Give the position of every Plasmodium parasite.
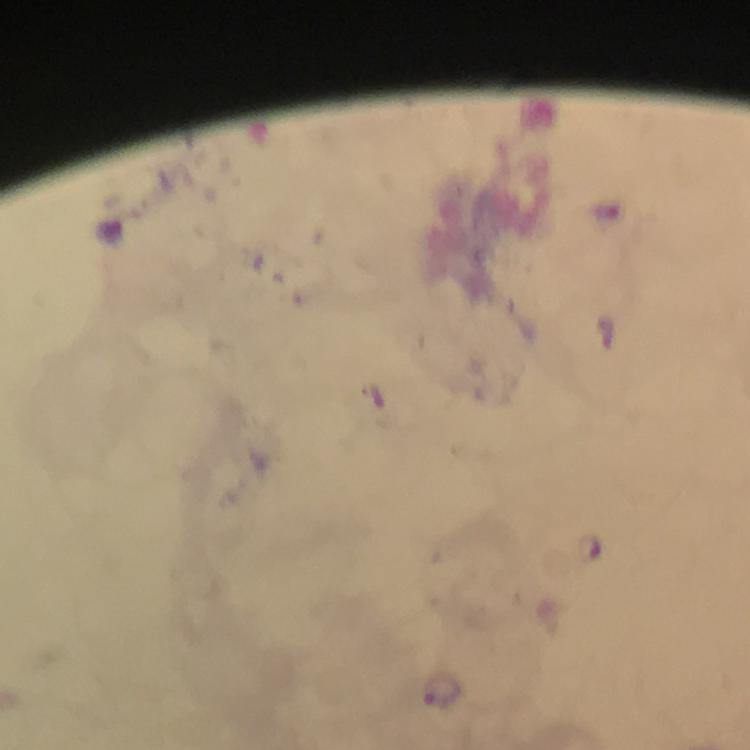

Approximate centers as [x, y] in pixels.
Plasmodium parasites: [441, 691].

cropped from = a single field of view
magnification = 100x
immersion oil = applied
context = from a malaria diagnostic workup
stain = Giemsa
capture = smartphone camera through the microscope
image size = 750×750 pixels
preparation = thick smear